Assess this cell for malaria.
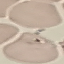
It is uninfected.

Summary:
  - Image type: automatically extracted cell patch, resized to 64 × 64 pixels
  - Preparation: thin blood film
  - Stain: Giemsa
  - Capture: smartphone camera at the microscope eyepiece